Outline platelets.
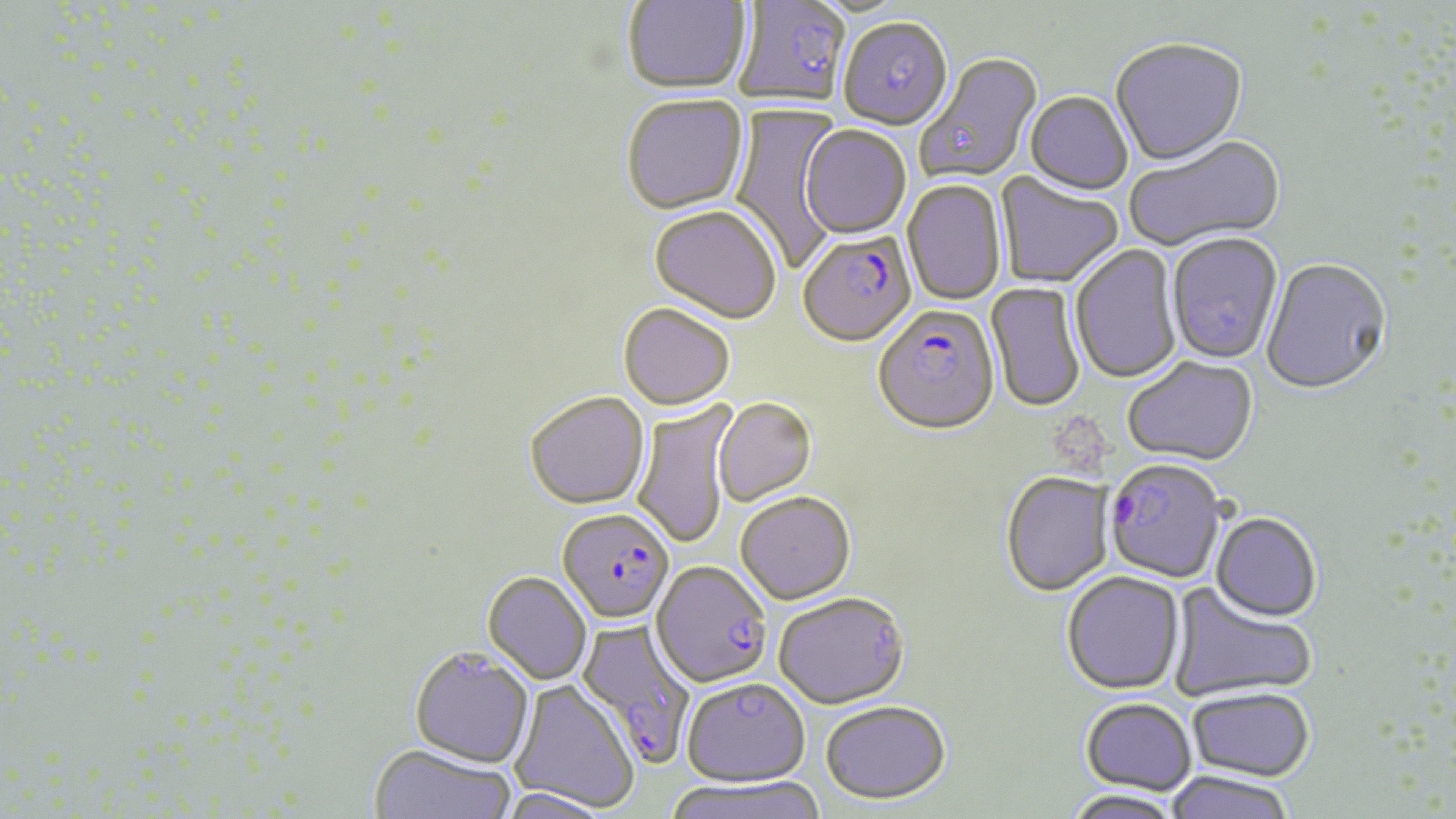
Approximate bounding boxes as (x1,y1)-(x2,y2) corner pairs in pixels.
Platelets: (1056,417)-(1120,477).

Summary:
  - Plasmodium falciparum-infected red blood cell locations: (798,232)-(917,349), (872,307)-(1000,438), (1104,460)-(1225,585), (557,508)-(674,624), (652,561)-(772,687), (576,619)-(697,768)
  - Uninfected red blood cell locations: (623,0)-(752,96), (733,1)-(850,112), (838,19)-(952,132), (1110,41)-(1248,169), (916,53)-(1043,185), (1024,93)-(1133,197), (622,96)-(749,217), (728,104)-(843,272), (800,126)-(910,241), (1125,135)-(1286,255), (994,173)-(1123,290), (902,180)-(1007,307), (649,208)-(781,326), (1166,234)-(1283,366), (1070,243)-(1182,386), (1260,260)-(1392,398), (985,281)-(1085,415), (618,305)-(735,411), (1122,358)-(1259,469), (524,391)-(650,510), (712,399)-(817,506), (631,401)-(738,550), (1000,473)-(1111,597), (735,492)-(856,604), (1210,515)-(1322,624), (482,571)-(592,685), (1062,572)-(1186,696), (1166,583)-(1315,703), (773,592)-(909,709), (409,645)-(535,767), (680,677)-(810,787), (510,679)-(640,813), (1187,687)-(1315,781), (1080,697)-(1198,795), (820,700)-(951,802), (367,743)-(517,819), (1163,771)-(1297,819), (664,776)-(826,819), (498,786)-(617,819), (1062,789)-(1186,819)
  - Slide-level diagnosis: Plasmodium falciparum
  - Image size: 1456×819 pixels
  - Field of view: one of a larger specimen
  - Modality: light microscopy
  - Stain: May-Grünwald-Giemsa
  - Magnification: 1000x
  - Preparation: thin blood smear